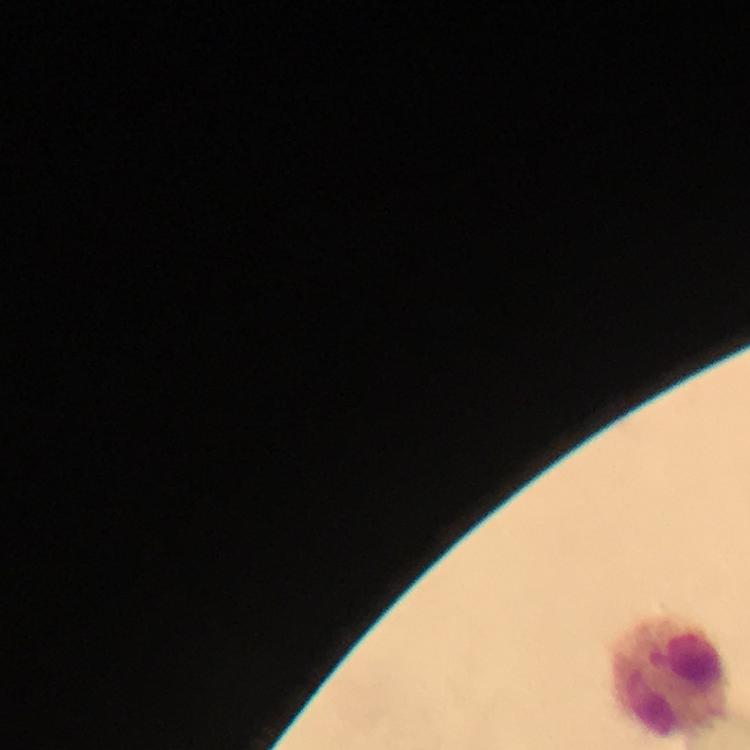

image_size: 750×750 pixels
malaria_parasites: none seen
immersion_oil: applied
stain: Giemsa
preparation: thick blood smear
magnification: 100x
cropped_from: one field of view
capture: smartphone photograph through a microscope
context: from a malaria diagnostic workup
leukocyte_locations: 'approximate object centers, in pixels from the top-left corner: (x=671, y=678)'